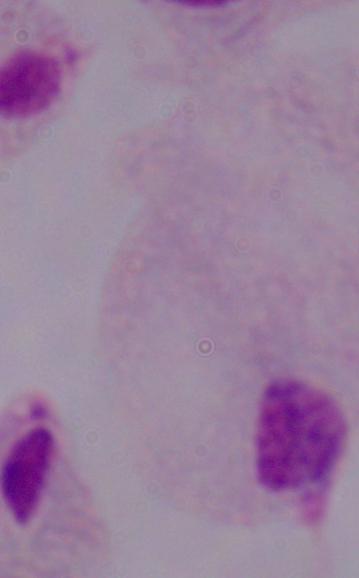
identification: trichomonad
modality: photomicrograph
magnification: 1000x